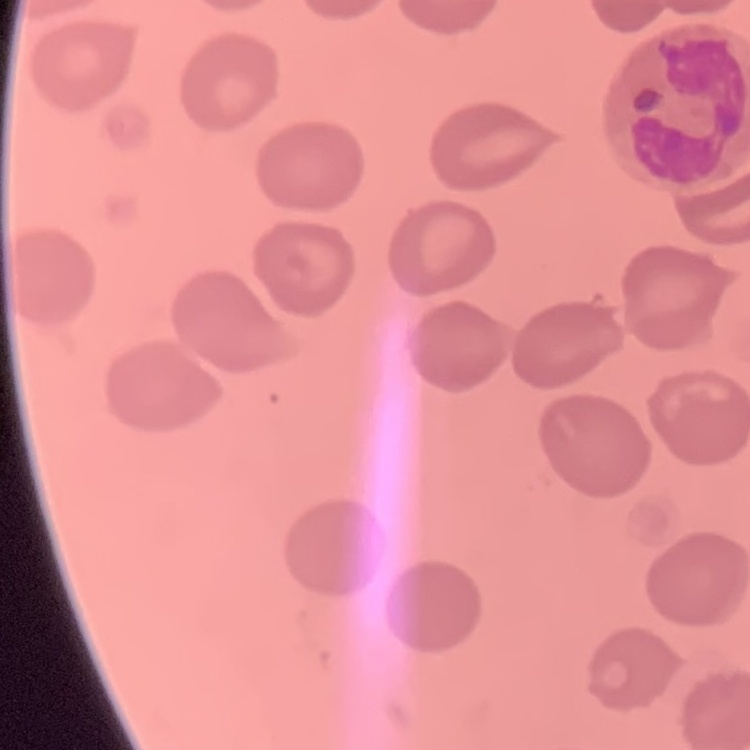
erythrocyte morphology = no rouleaux formation
stain = Field's or Giemsa
preparation = thin blood smear
image type = one tile cut from a larger photomicrograph